Report the malaria status of this cell.
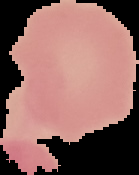

Uninfected.

From a thin blood smear. Segmented cell region on a black background. Image is 139×175 pixels.